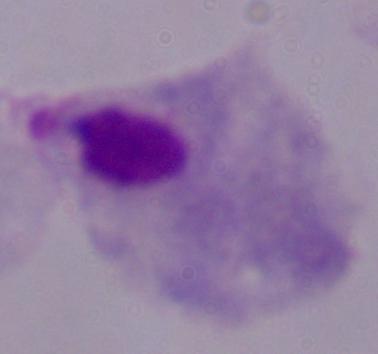

magnification = 1000x
identification = trichomonad
modality = micrograph